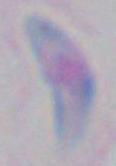 Photomicrograph. 1000x magnification. Toxoplasma gondii is seen.